State which parasite is depicted.
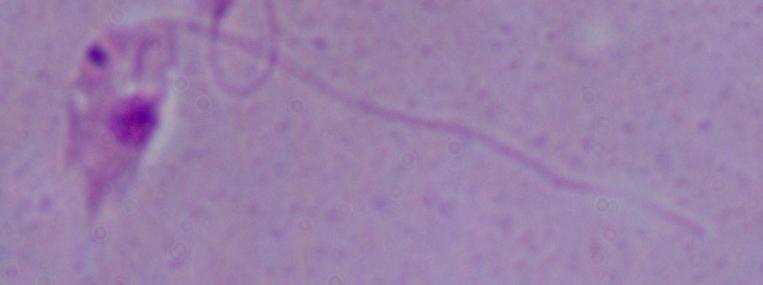

This is Leishmania.

1000x magnification. Photomicrograph.